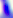
Summary:
  - Magnification: 400x
  - Modality: micrograph
  - Identification: Toxoplasma gondii